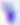
Summary:
  - Identification: Toxoplasma gondii
  - Modality: micrograph
  - Magnification: 400x